Assess this cell for malaria.
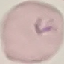
Parasitized.

preparation: thin blood film
stain: Giemsa
image_type: cell patch, automatically extracted from a larger field of view and resized to 64 × 64 pixels
capture: smartphone through the microscope eyepiece